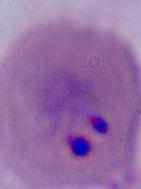
Micrograph. 400x or 1000x magnification. A Plasmodium parasite is seen.